Outline each Plasmodium vivax-infected red blood cell.
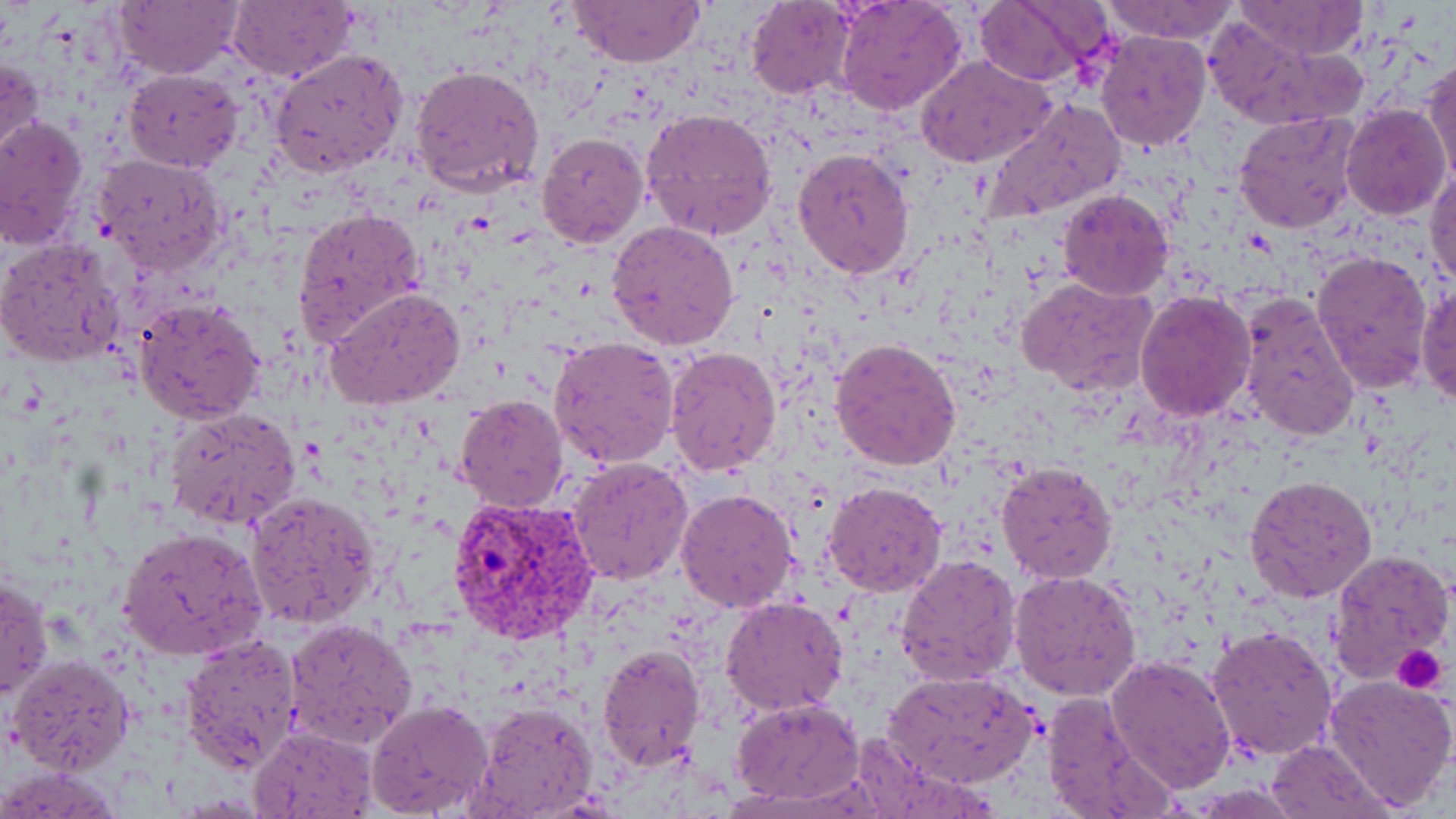
Approximate bounding boxes as (x1,y1)-(x2,y2) corner pairs in pixels.
Plasmodium vivax-infected red blood cells: (445,494)-(598,645).

Platelet locations: (1392,642)-(1451,694). Uninfected red blood cell locations: (228,0)-(357,82), (1100,0)-(1242,46), (112,1)-(244,80), (564,1)-(708,68), (746,1)-(858,98), (834,1)-(966,115), (970,1)-(1104,85), (1236,3)-(1366,61), (1206,20)-(1351,129), (1098,32)-(1211,151), (270,48)-(409,176), (0,56)-(45,165), (918,56)-(1057,168), (1421,58)-(1456,186), (411,63)-(546,198), (123,69)-(243,172), (979,96)-(1124,227), (1342,103)-(1450,218), (642,107)-(778,240), (1233,110)-(1362,233), (0,114)-(88,248), (536,130)-(649,247), (792,148)-(914,279), (95,155)-(230,273), (1426,167)-(1456,293), (1058,188)-(1173,301), (291,206)-(427,344), (607,220)-(740,351), (0,237)-(126,370), (1310,250)-(1435,395), (1017,277)-(1157,396), (1416,281)-(1456,407), (327,286)-(466,408), (1234,291)-(1361,444), (1134,292)-(1257,422), (134,295)-(265,426), (548,336)-(679,470), (830,336)-(962,473), (663,346)-(782,478), (455,393)-(570,513), (165,408)-(302,530), (567,455)-(693,586), (996,460)-(1119,584), (1245,476)-(1378,602), (823,480)-(948,597), (676,488)-(799,611), (244,489)-(382,628), (118,527)-(271,661), (1327,547)-(1453,685), (896,554)-(1022,685), (1010,568)-(1143,702), (0,573)-(52,701), (720,596)-(849,717), (286,618)-(418,751), (1205,624)-(1338,762), (180,631)-(304,773), (595,642)-(706,771), (8,653)-(135,774), (1106,654)-(1236,794), (886,670)-(1038,790), (1324,673)-(1456,809), (1038,691)-(1171,819), (732,697)-(863,805), (367,699)-(495,819), (473,700)-(602,819), (249,725)-(376,818), (1266,739)-(1394,818), (0,764)-(125,817). Slide-level diagnosis: Plasmodium vivax. 1000x magnification. One field of a larger specimen. Optical microscopy. Thin blood smear. May-Grünwald-Giemsa stain. Image is 1456×819 pixels.